Mark where leukocytes are.
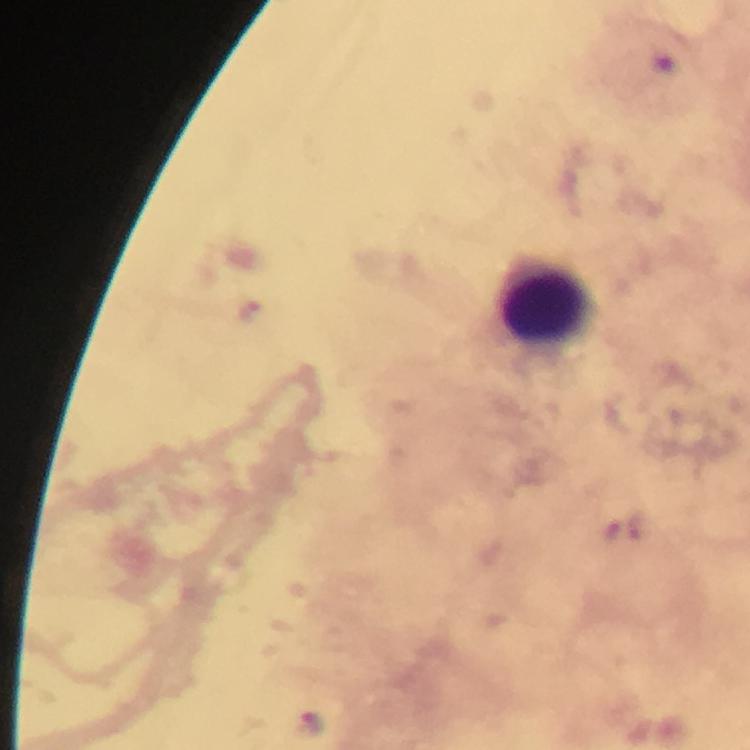
Approximate centers as [x, y] in pixels.
Leukocytes: [546, 306].

Summary:
  - Malaria parasite locations: [250, 311], [311, 721]
  - Immersion oil: applied
  - Magnification: 100x
  - Preparation: thick blood smear
  - Stain: Giemsa
  - Context: from a diagnostic examination for malaria
  - Capture: smartphone camera through the microscope
  - Image size: 750×750 pixels
  - Cropped from: a single field of view